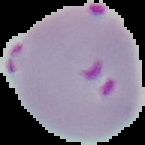

Summary:
  - Image type: segmented cell region with the area outside set to black
  - Malaria status: parasitized
  - Preparation: thin blood film
  - Image size: 145×145 pixels